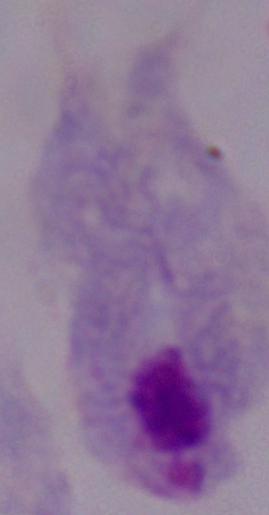

modality: photomicrograph
identification: trichomonad
magnification: 1000x